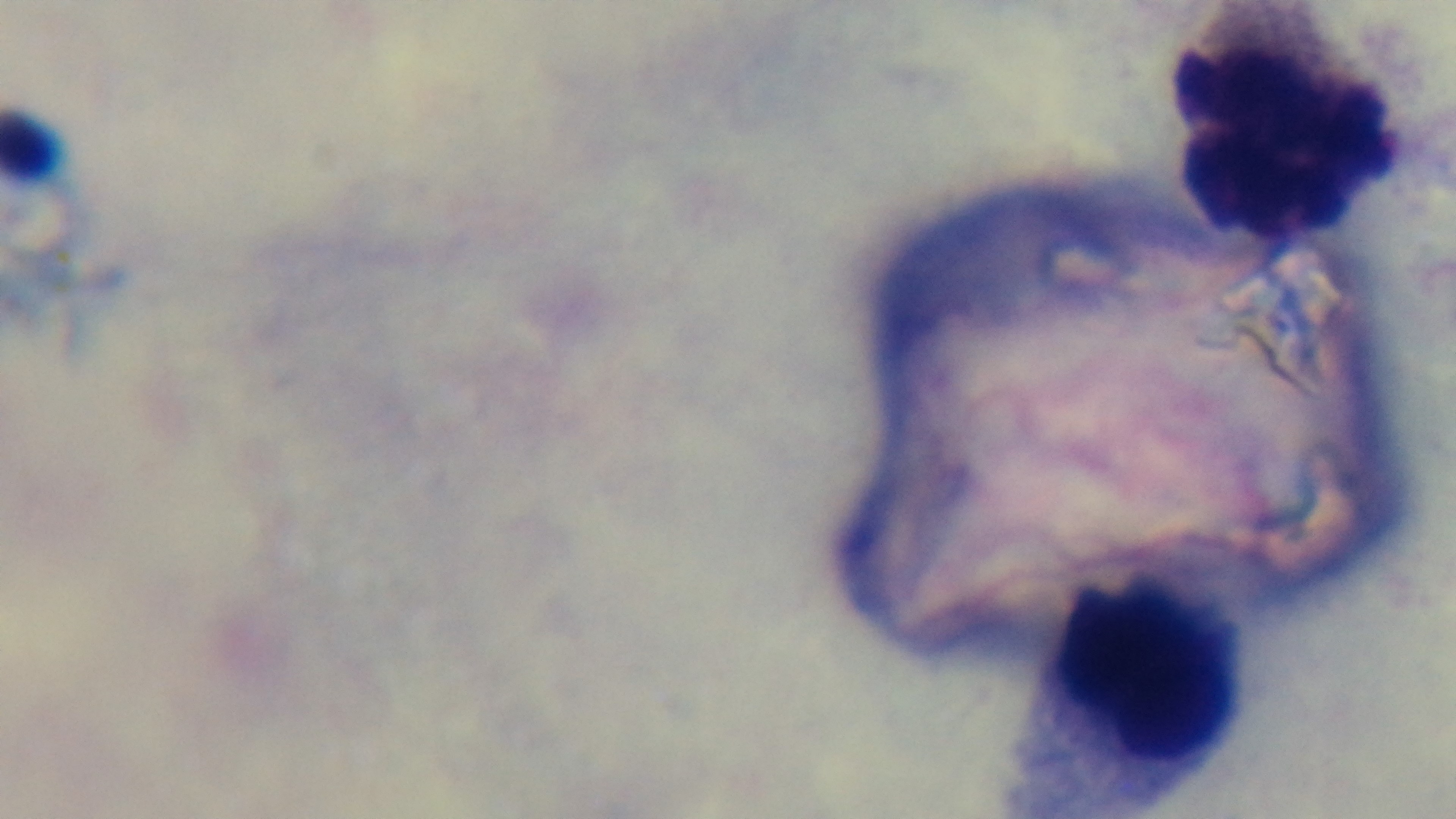 Giemsa stain. Oil-immersion objective, 100x. Malaria status: uninfected. Preparation: thick blood film. Photomicrograph. Captured with a mounted 4K digital camera. Single field of view.